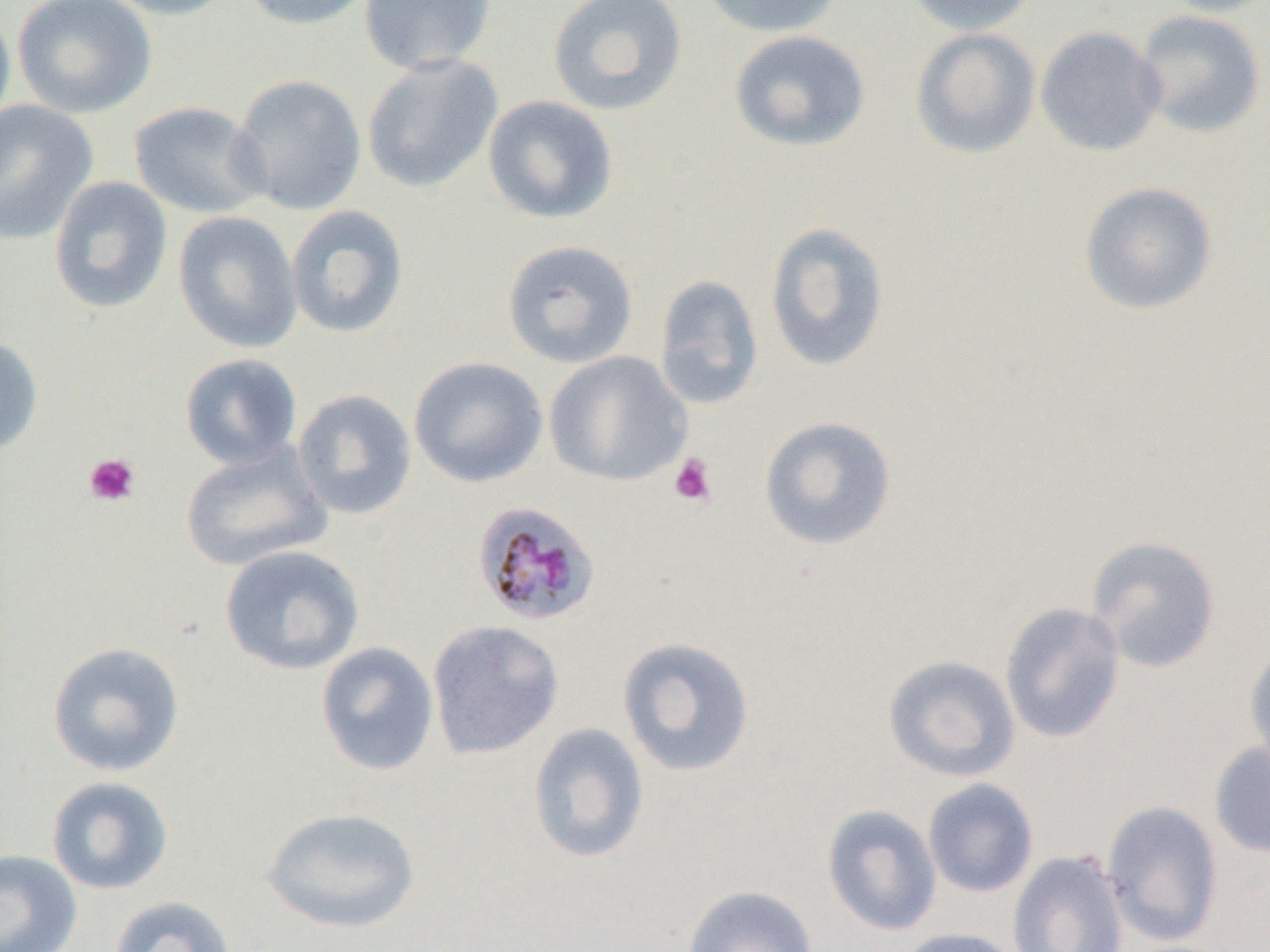 Approximate bounding boxes as [x1, y1, x2, y2] in pixels. Uninfected red blood cell locations: [13, 0, 156, 119], [98, 0, 238, 20], [237, 0, 378, 30], [358, 0, 497, 76], [547, 0, 688, 117], [697, 0, 842, 38], [905, 0, 1041, 35], [1155, 0, 1270, 17], [0, 2, 16, 139], [1133, 10, 1267, 139], [1035, 25, 1166, 157], [910, 28, 1042, 159], [729, 30, 871, 153], [361, 54, 503, 193], [230, 74, 367, 216], [483, 95, 618, 224], [0, 99, 99, 245], [128, 101, 271, 219], [48, 176, 173, 315], [1078, 181, 1218, 316], [285, 204, 410, 339], [173, 211, 302, 354], [764, 221, 890, 372], [501, 239, 638, 369], [654, 274, 764, 410], [0, 334, 44, 458], [543, 351, 692, 487], [180, 353, 302, 470], [409, 356, 548, 488], [292, 389, 417, 520], [759, 416, 897, 551], [180, 443, 331, 572], [1085, 534, 1222, 673], [219, 545, 365, 675], [1000, 601, 1125, 744], [427, 619, 564, 760], [617, 636, 756, 778], [47, 641, 185, 777], [315, 641, 439, 777], [1243, 641, 1270, 774], [883, 654, 1021, 782], [527, 722, 650, 864], [1209, 739, 1270, 858], [46, 776, 174, 896], [922, 778, 1039, 898], [1101, 801, 1224, 947], [822, 804, 943, 937], [261, 806, 421, 934], [0, 849, 82, 952], [1007, 849, 1129, 952], [682, 885, 819, 952], [108, 895, 238, 952], [890, 927, 1026, 952]. Platelet locations: [84, 453, 140, 507], [668, 453, 717, 507]. Plasmodium malariae-infected red blood cell locations: [471, 500, 601, 627]. Slide-level diagnosis: Plasmodium malariae. 1000x magnification. Optical microscopy. Single field of view. Image is 1270×952 pixels. Thin blood smear.